Identify the parasite.
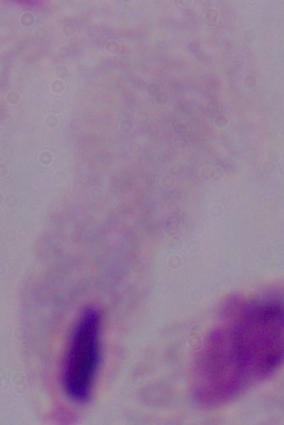
This is a trichomonad.

modality = micrograph
magnification = 1000x